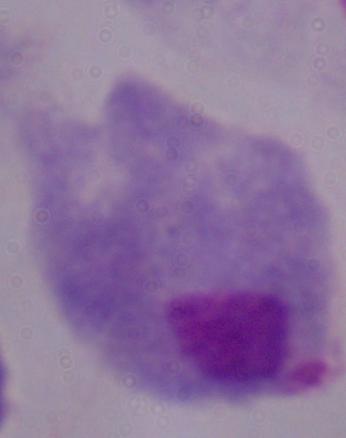
Summary:
  - Identification: trichomonad
  - Magnification: 1000x
  - Modality: photomicrograph